Locate every Plasmodium falciparum-infected red blood cell.
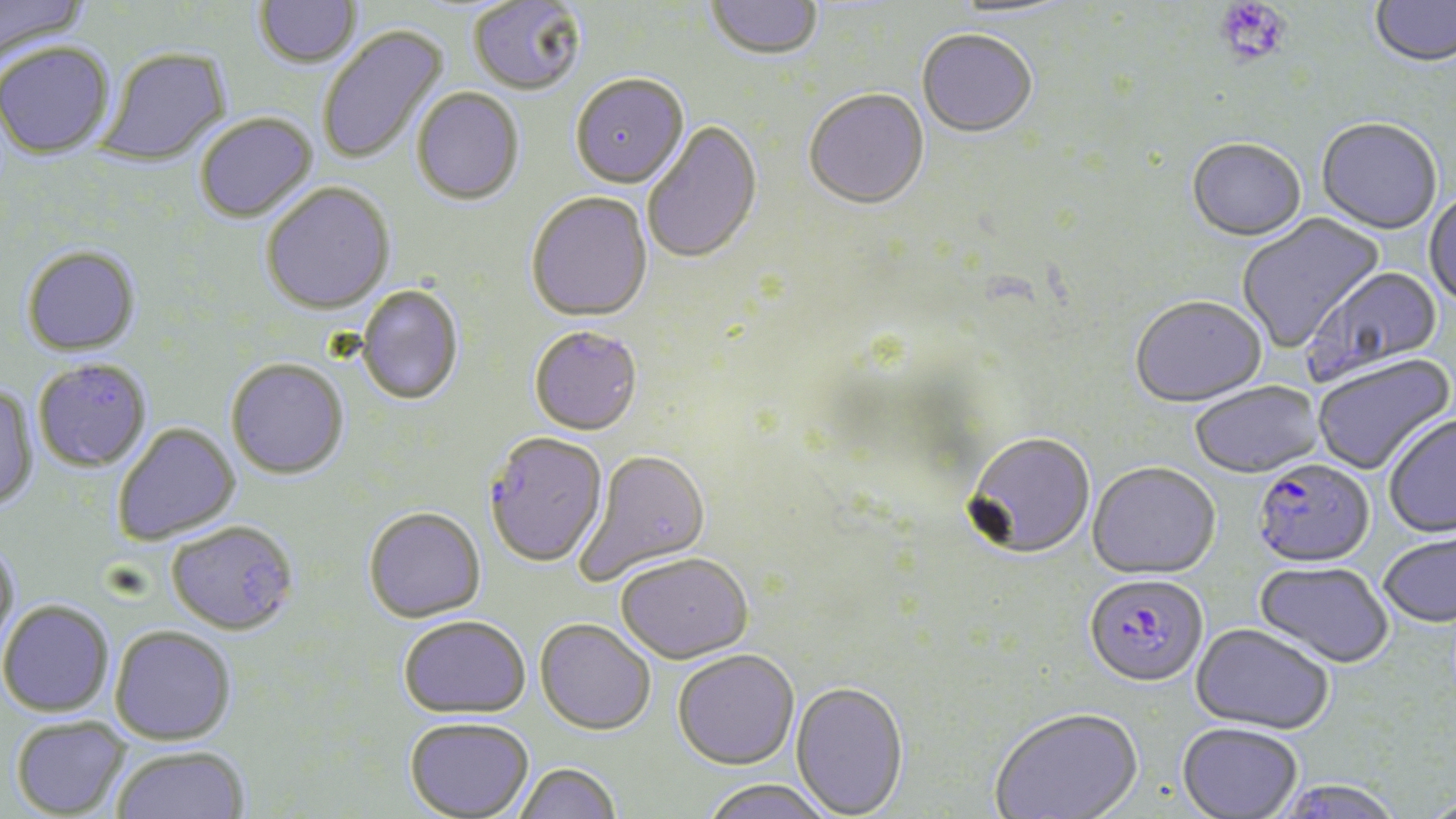

Approximate bounding boxes as (x1, y1, x2, y2) in pixels.
Plasmodium falciparum-infected red blood cells: (484, 434, 608, 570), (1251, 460, 1375, 571), (1084, 577, 1208, 691).

slide-level diagnosis = Plasmodium falciparum
platelet locations = approximate bounding boxes as (x1, y1, x2, y2) in pixels: (1215, 1, 1291, 69)
modality = light microscopy
field of view = one of a larger specimen
preparation = thin blood film
image size = 1456×819 pixels
magnification = 1000x
uninfected red blood cell locations = approximate bounding boxes as (x1, y1, x2, y2) in pixels: (0, 0, 90, 63), (254, 0, 362, 72), (1370, 0, 1456, 70), (469, 1, 586, 98), (705, 1, 823, 64), (943, 1, 1074, 23), (317, 23, 450, 166), (917, 32, 1037, 141), (0, 43, 115, 161), (98, 49, 232, 167), (570, 76, 689, 191), (412, 89, 524, 208), (804, 91, 930, 213), (195, 114, 318, 225), (1316, 121, 1443, 237), (642, 122, 764, 266), (1186, 140, 1307, 245), (261, 184, 395, 318), (1424, 192, 1456, 310), (525, 194, 653, 325), (1237, 212, 1385, 354), (21, 245, 141, 357), (1303, 266, 1444, 386), (357, 286, 464, 407), (1130, 298, 1267, 410), (529, 328, 643, 438), (1313, 355, 1455, 476), (33, 358, 152, 472), (226, 360, 349, 482), (1190, 382, 1325, 480), (0, 384, 39, 512), (1384, 416, 1456, 539), (113, 423, 240, 545), (962, 435, 1095, 562), (575, 451, 712, 586), (1087, 464, 1221, 582), (364, 509, 486, 626), (166, 523, 298, 637), (1379, 532, 1455, 629), (0, 539, 20, 659), (616, 556, 754, 666), (1254, 563, 1394, 670), (0, 600, 114, 717), (398, 619, 531, 722), (534, 621, 655, 738), (1191, 625, 1334, 737), (109, 626, 237, 746), (672, 652, 800, 773), (790, 683, 909, 818), (990, 709, 1144, 819), (11, 716, 131, 818), (404, 720, 534, 819), (1176, 724, 1303, 818), (112, 746, 250, 819), (515, 765, 622, 819), (1269, 779, 1406, 819), (700, 782, 834, 819)
stain = May-Grünwald-Giemsa